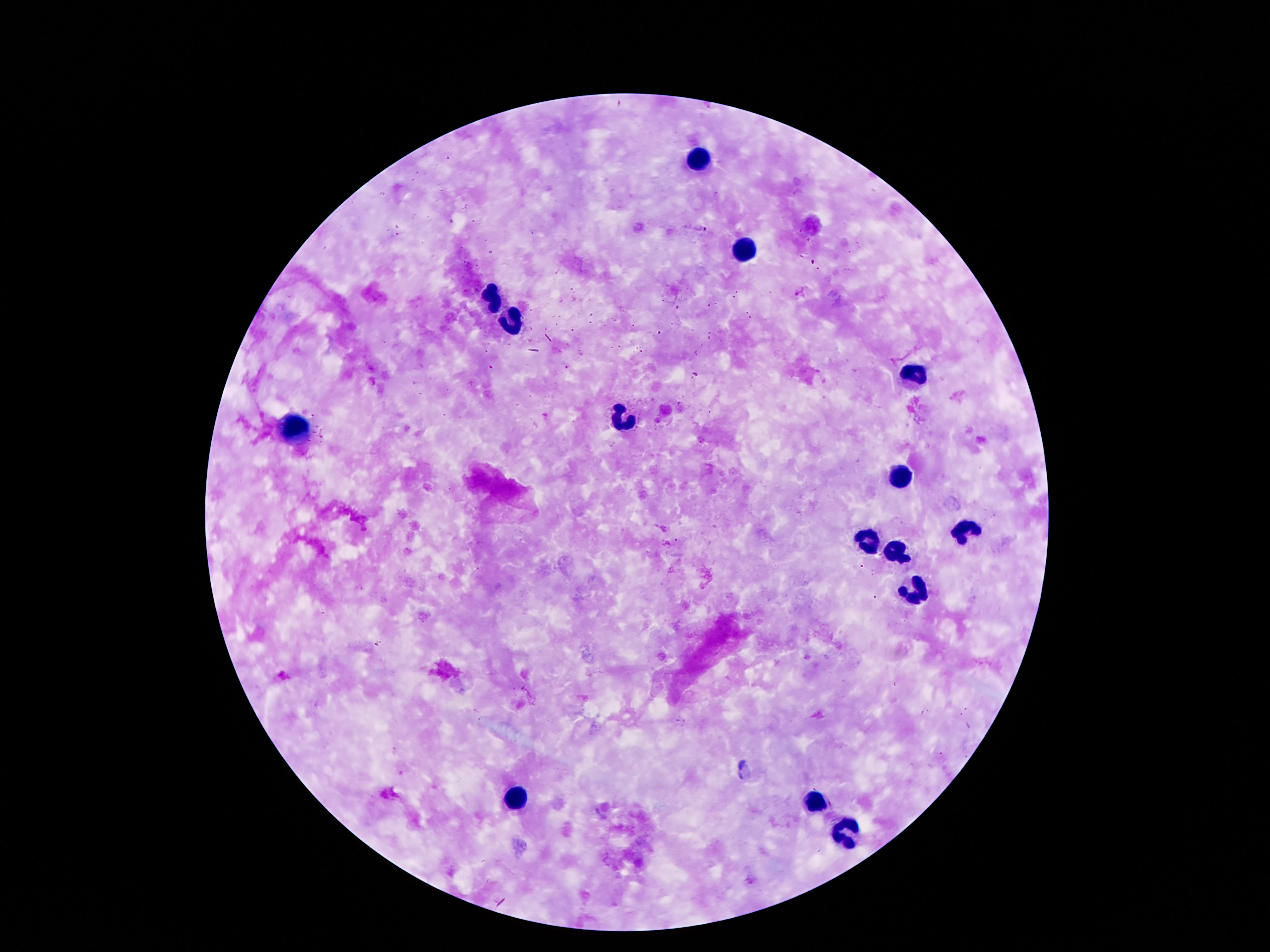

Approximate centers as [x, y] in pixels. Leukocyte locations: [696, 160], [747, 249], [493, 293], [510, 323], [915, 375], [617, 419], [293, 425], [906, 474], [965, 533], [866, 543], [896, 552], [915, 592], [514, 800], [810, 805], [847, 830]. Image is 1270×952 pixels. Thick blood film. 100x magnification. Giemsa stain. Single field of view. Patient malaria status: negative. Smartphone photograph taken through the microscope eyepiece.